Name the parasite shown.
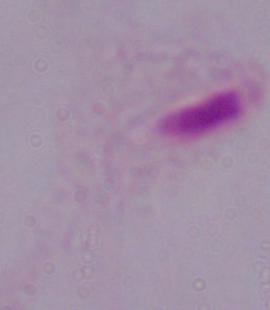

A trichomonad.

magnification: 1000x
modality: micrograph